Report the malaria status of this cell.
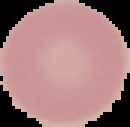

It is uninfected.

Image is 130×127 pixels. From a thin blood smear. Cell region segmented out of the field of view; the surrounding area is masked to black.